State the blood parasite species.
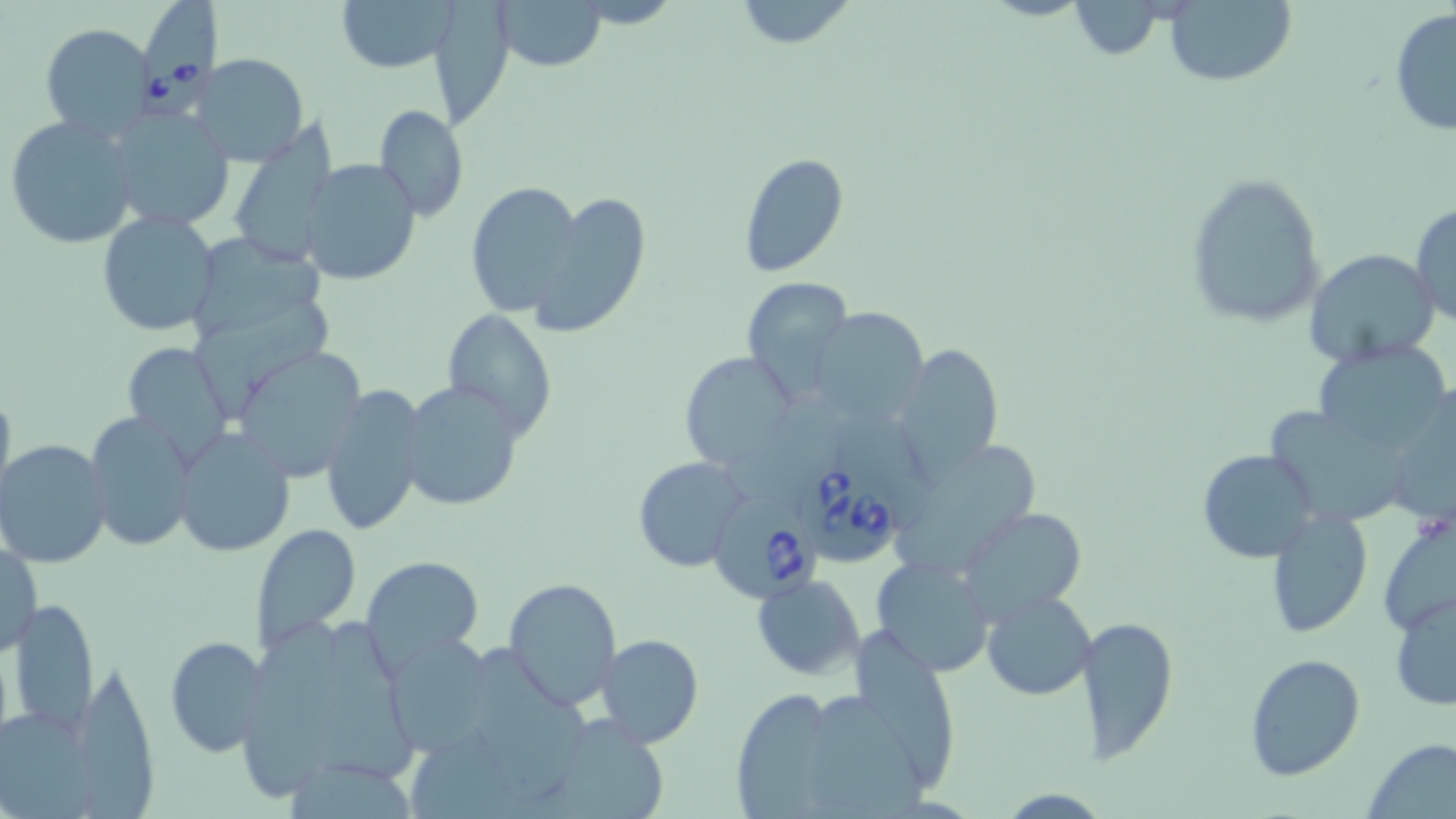
Babesia divergens.

Approximate bounding boxes as [x1, y1, x2, y2] in pixels. Babesia divergens-infected red blood cell locations: [138, 2, 218, 106], [798, 464, 903, 569], [710, 490, 819, 598]. Uninfected red blood cell locations: [333, 0, 465, 73], [431, 0, 519, 132], [498, 0, 606, 73], [733, 0, 859, 51], [1063, 0, 1170, 58], [1164, 0, 1296, 86], [1389, 9, 1456, 137], [41, 24, 155, 140], [194, 55, 310, 167], [106, 104, 233, 231], [374, 104, 469, 221], [4, 115, 139, 251], [230, 135, 336, 269], [738, 153, 849, 276], [297, 160, 421, 287], [1183, 171, 1326, 326], [465, 181, 582, 316], [535, 192, 652, 335], [1409, 203, 1456, 327], [97, 210, 220, 337], [194, 228, 330, 343], [1304, 248, 1439, 369], [740, 276, 851, 393], [192, 307, 334, 418], [807, 307, 928, 424], [442, 310, 555, 439], [120, 339, 234, 460], [1311, 343, 1453, 454], [897, 345, 1004, 478], [678, 350, 796, 473], [238, 351, 362, 481], [396, 380, 524, 512], [319, 383, 428, 537], [0, 386, 16, 505], [1384, 392, 1456, 528], [1266, 405, 1396, 523], [84, 413, 196, 553], [172, 427, 296, 558], [1, 438, 114, 568], [1198, 449, 1320, 563], [901, 450, 1042, 559], [633, 457, 749, 573], [957, 505, 1088, 624], [1265, 509, 1372, 636], [1379, 510, 1456, 637], [249, 523, 362, 655], [2, 541, 42, 655], [361, 554, 482, 670], [870, 555, 993, 677], [503, 575, 623, 708], [753, 575, 865, 678], [982, 587, 1096, 700], [1389, 591, 1455, 711], [10, 598, 97, 737], [233, 601, 340, 797], [1075, 611, 1179, 765], [323, 621, 422, 784], [854, 624, 968, 784], [385, 632, 499, 756], [595, 634, 703, 748], [164, 636, 271, 758], [472, 644, 594, 789], [1245, 652, 1365, 779], [84, 668, 160, 819], [739, 689, 832, 819], [823, 693, 938, 819], [0, 706, 103, 819], [537, 715, 675, 819], [413, 736, 545, 819], [1364, 738, 1456, 818], [281, 746, 428, 819]. May-Grünwald-Giemsa stain. Single field of view. Captured at 1000x magnification. Thin blood smear. Optical microscopy. Image is 1456×819 pixels.